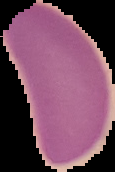 Image is 115×172 pixels. Cell region segmented out of the field of view; the surrounding area is masked to black. Result: negative for malaria parasites. From a thin blood smear.